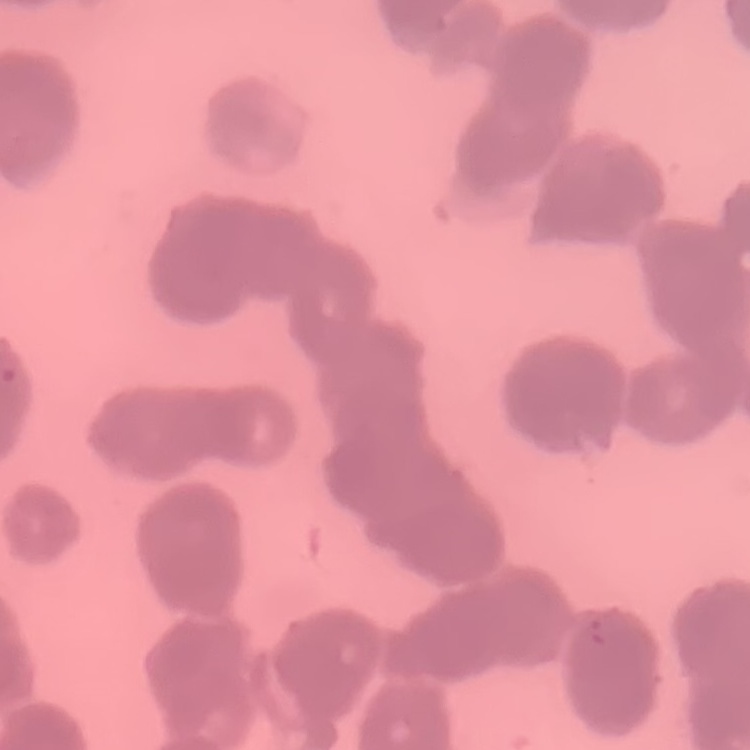

{
  "red_blood_cell_morphology": "rouleaux formation",
  "image_type": "square crop of a larger photomicrograph",
  "stain": "Field's or Giemsa",
  "preparation": "thin blood smear"
}